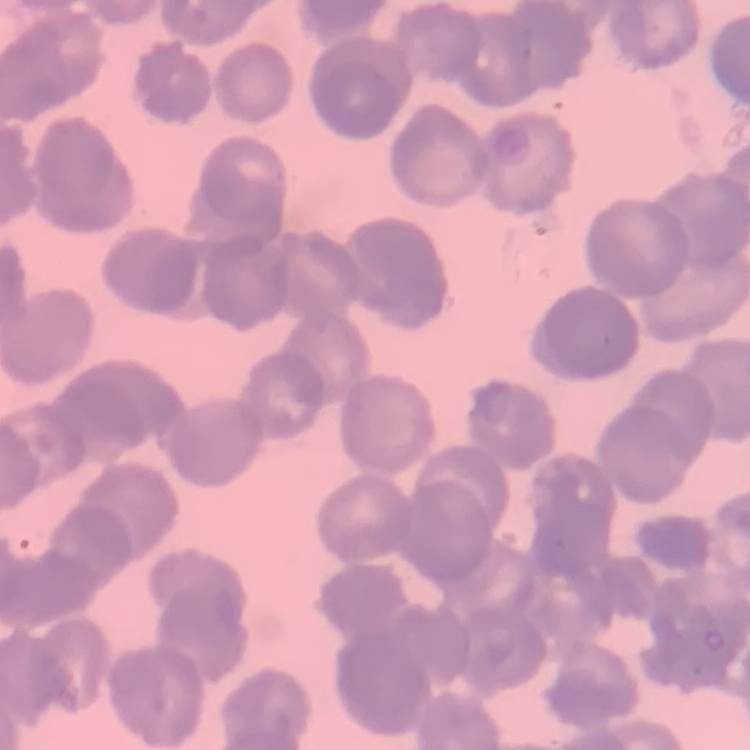

The red blood cells exhibit rouleaux formation. One tile cut from a larger photomicrograph. Field's or Giemsa stain. Thin peripheral smear.